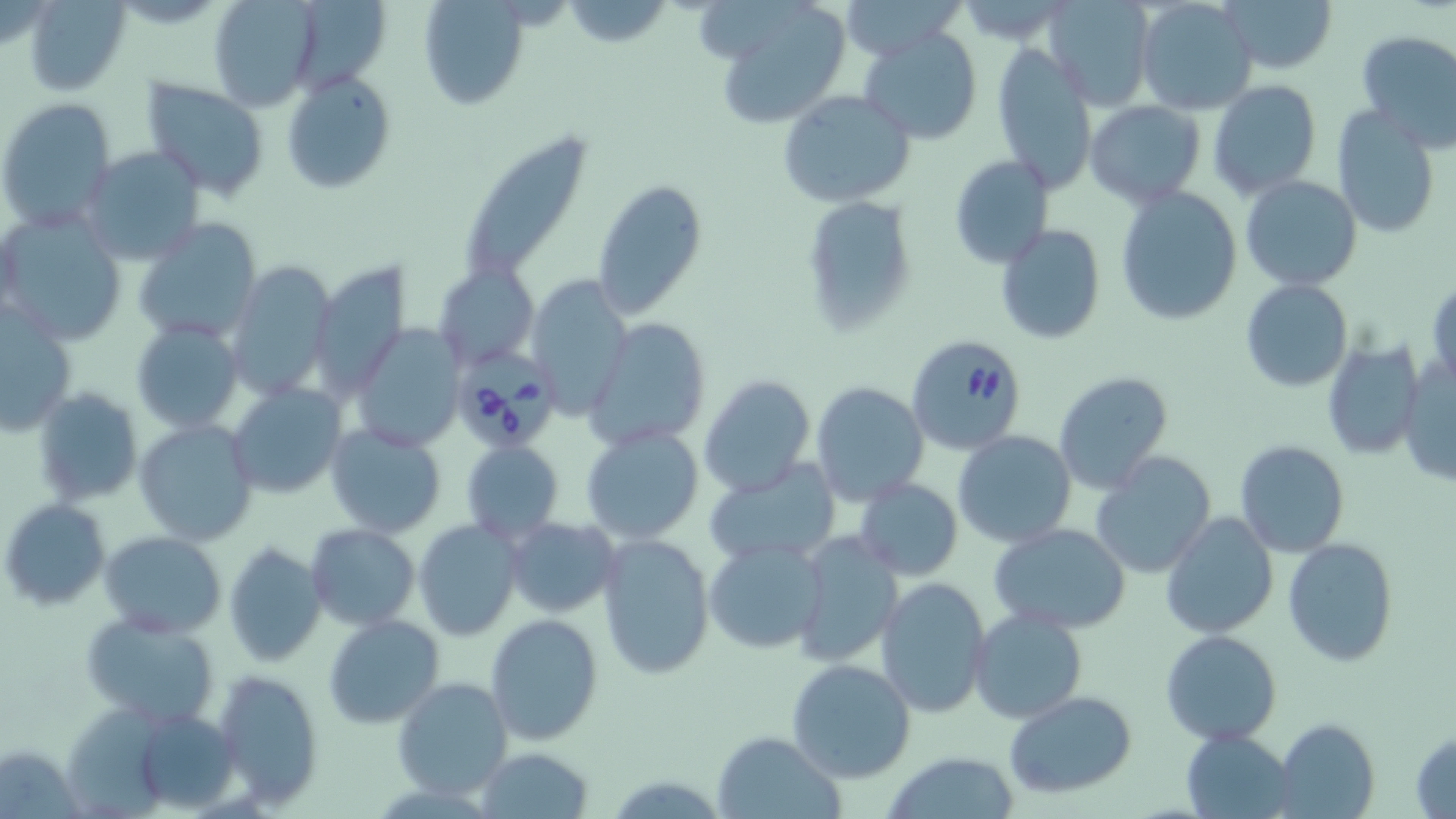

Approximate bounding boxes as (x1, y1, x2, y2) in pixels. Babesia divergens-infected red blood cell locations: (905, 335, 1028, 454), (453, 359, 551, 448). Uninfected red blood cell locations: (22, 0, 132, 96), (208, 0, 320, 108), (417, 0, 530, 110), (842, 0, 958, 59), (1134, 0, 1259, 116), (1221, 0, 1336, 75), (300, 1, 394, 94), (1044, 1, 1153, 110), (564, 2, 670, 48), (724, 5, 849, 128), (858, 28, 984, 145), (1355, 29, 1456, 152), (990, 44, 1098, 192), (282, 70, 397, 195), (141, 78, 270, 198), (1207, 81, 1323, 200), (777, 91, 917, 208), (1, 98, 117, 230), (1085, 100, 1206, 206), (1332, 106, 1442, 239), (469, 138, 595, 278), (78, 146, 205, 266), (948, 155, 1055, 268), (1240, 175, 1362, 292), (590, 178, 707, 320), (1115, 184, 1244, 324), (800, 195, 918, 337), (0, 210, 126, 346), (132, 216, 261, 344), (994, 223, 1107, 346), (225, 261, 334, 398), (436, 263, 534, 371), (309, 264, 409, 407), (529, 277, 630, 414), (1241, 280, 1352, 392), (1427, 280, 1455, 392), (1, 309, 76, 434), (587, 318, 710, 449), (131, 320, 243, 435), (352, 325, 465, 452), (1321, 339, 1425, 460), (1399, 356, 1454, 490), (1052, 372, 1176, 495), (697, 375, 815, 498), (810, 380, 929, 505), (227, 384, 346, 499), (33, 385, 143, 506), (135, 418, 258, 545), (324, 423, 447, 538), (581, 425, 704, 544), (953, 431, 1076, 547), (1233, 439, 1351, 558), (461, 440, 564, 545), (1090, 453, 1216, 578), (704, 459, 842, 568), (853, 478, 963, 581), (3, 499, 110, 608), (1160, 513, 1279, 639), (505, 517, 620, 619), (413, 520, 523, 641), (991, 523, 1133, 633), (305, 524, 420, 630), (101, 530, 226, 637), (596, 531, 716, 681), (792, 533, 903, 668), (704, 538, 829, 655), (1283, 538, 1398, 666), (224, 543, 328, 668), (876, 578, 992, 716), (970, 608, 1088, 725), (80, 611, 222, 731), (484, 613, 604, 744), (324, 615, 446, 729), (1161, 630, 1284, 746), (786, 658, 916, 783), (211, 669, 323, 808), (392, 674, 514, 800), (1004, 690, 1136, 798), (66, 700, 175, 819), (115, 705, 247, 814), (1277, 718, 1380, 819), (1181, 729, 1299, 819), (1409, 729, 1456, 817), (712, 730, 844, 819), (475, 746, 594, 818), (880, 750, 1023, 819). Slide-level diagnosis: Babesia divergens. Thin blood smear. 1000x magnification. Optical microscopy. Image is 1456×819 pixels. One field of a larger specimen. May-Grünwald-Giemsa-stained preparation.